Report the malaria status of this cell.
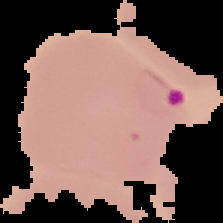

It is parasitized.

Image is 223×223 pixels. From a thin blood film. The area outside the segmented cell region is set to black.